State the blood parasite species.
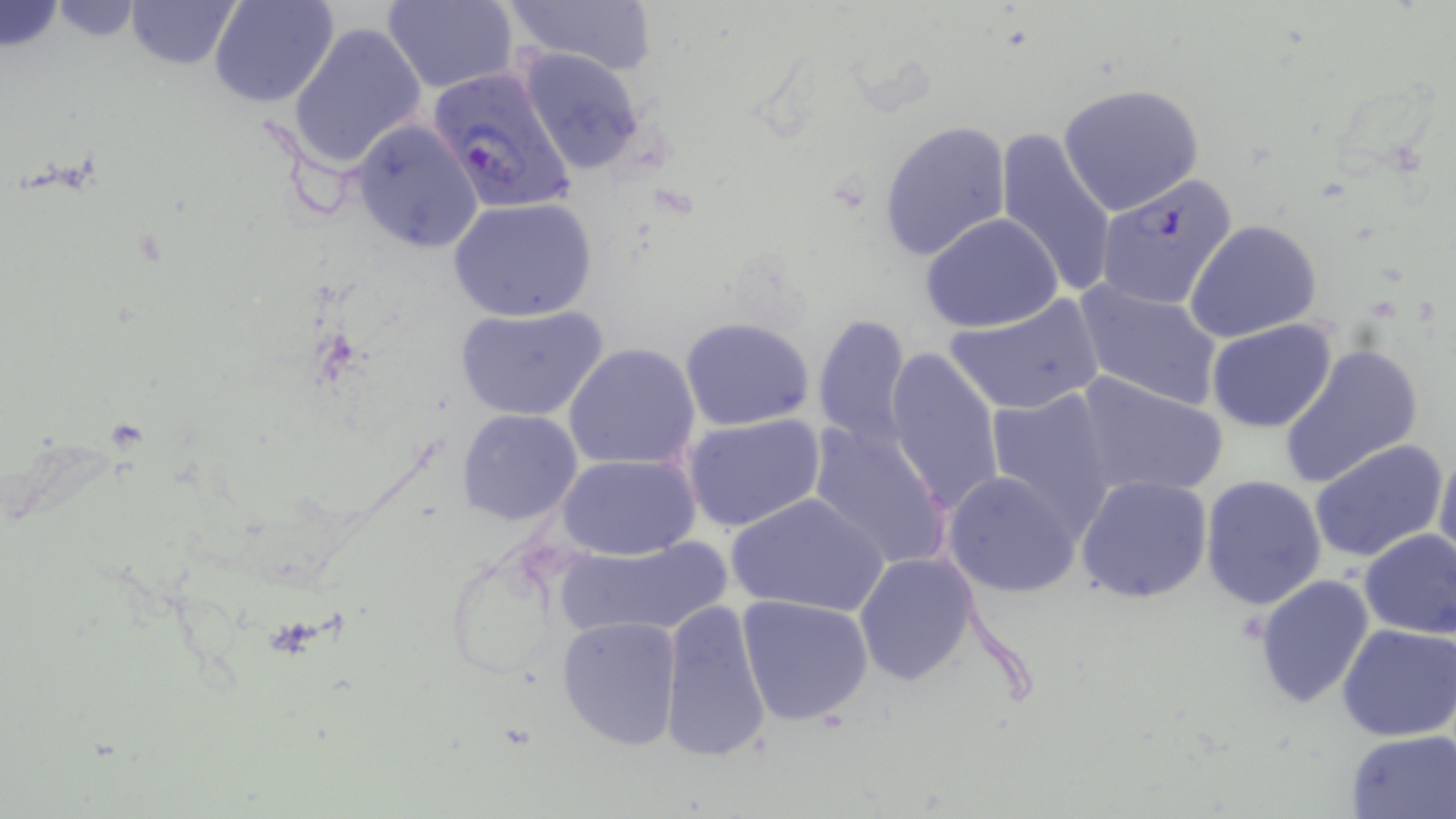

Plasmodium falciparum.

Summary:
  - Coordinate format: approximate bounding boxes as named x1/y1/x2/y2 corners in pixels
  - Plasmodium falciparum-infected red blood cell locations: (x1=427, y1=64, x2=577, y2=215), (x1=1094, y1=172, x2=1239, y2=310)
  - Uninfected red blood cell locations: (x1=124, y1=0, x2=244, y2=70), (x1=210, y1=0, x2=341, y2=108), (x1=380, y1=0, x2=518, y2=92), (x1=495, y1=0, x2=659, y2=74), (x1=287, y1=20, x2=427, y2=170), (x1=518, y1=47, x2=650, y2=176), (x1=1058, y1=83, x2=1204, y2=215), (x1=350, y1=118, x2=485, y2=253), (x1=878, y1=120, x2=1012, y2=262), (x1=993, y1=128, x2=1121, y2=300), (x1=450, y1=198, x2=597, y2=322), (x1=921, y1=213, x2=1064, y2=332), (x1=1185, y1=219, x2=1322, y2=343), (x1=1075, y1=279, x2=1225, y2=409), (x1=943, y1=295, x2=1106, y2=415), (x1=455, y1=303, x2=607, y2=423), (x1=813, y1=314, x2=913, y2=448), (x1=680, y1=317, x2=814, y2=431), (x1=1206, y1=319, x2=1339, y2=433), (x1=563, y1=343, x2=701, y2=472), (x1=1279, y1=343, x2=1426, y2=487), (x1=884, y1=345, x2=1007, y2=516), (x1=1073, y1=372, x2=1228, y2=498), (x1=984, y1=387, x2=1121, y2=536), (x1=458, y1=409, x2=583, y2=526), (x1=681, y1=413, x2=826, y2=534), (x1=805, y1=421, x2=954, y2=572), (x1=1309, y1=440, x2=1449, y2=565), (x1=1435, y1=442, x2=1456, y2=571), (x1=558, y1=453, x2=699, y2=560), (x1=943, y1=471, x2=1081, y2=597), (x1=1199, y1=474, x2=1326, y2=610), (x1=1076, y1=475, x2=1213, y2=603), (x1=727, y1=489, x2=888, y2=619), (x1=1357, y1=528, x2=1456, y2=639), (x1=551, y1=538, x2=732, y2=643), (x1=852, y1=551, x2=979, y2=685), (x1=1253, y1=574, x2=1375, y2=709), (x1=735, y1=593, x2=876, y2=726), (x1=658, y1=599, x2=773, y2=764), (x1=556, y1=616, x2=682, y2=751), (x1=1337, y1=622, x2=1456, y2=741), (x1=1346, y1=729, x2=1456, y2=817)
  - Stain: May-Grünwald-Giemsa
  - Field of view: one of a larger specimen
  - Preparation: thin blood film
  - Image size: 1456×819 pixels
  - Magnification: 1000x
  - Modality: light microscopy